Assess the morphology of the red blood cells.
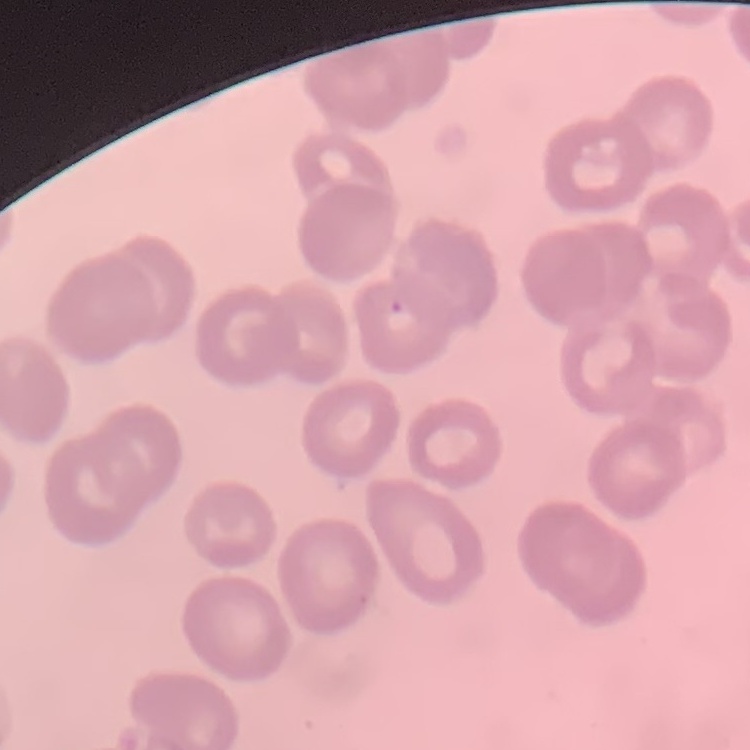

They show no rouleaux formation.

preparation = thin blood film
stain = Field's or Giemsa
image type = one tile cut from a larger photomicrograph